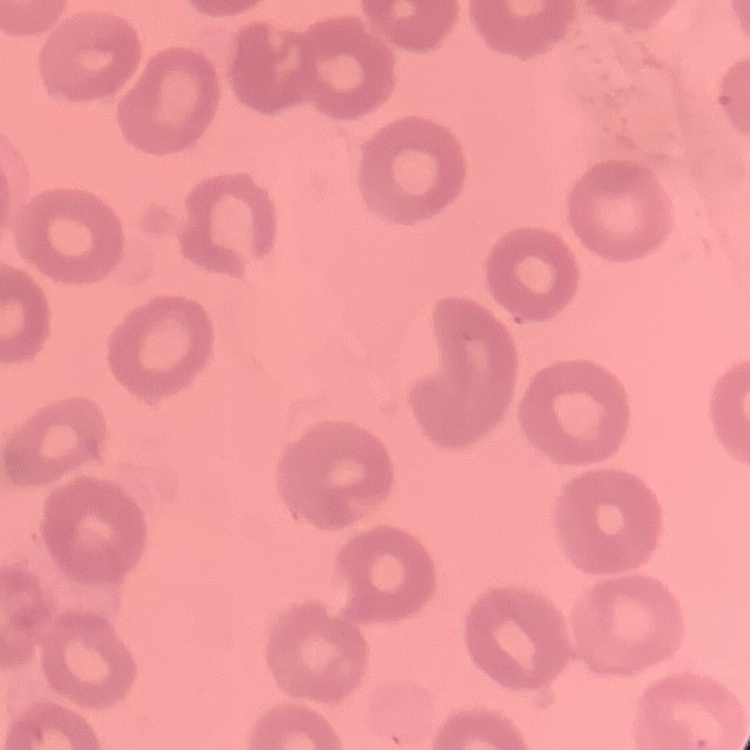

The erythrocytes exhibit no rouleaux formation. Stained with either Field's or Giemsa. One tile cut from a larger photomicrograph. Thin blood film.